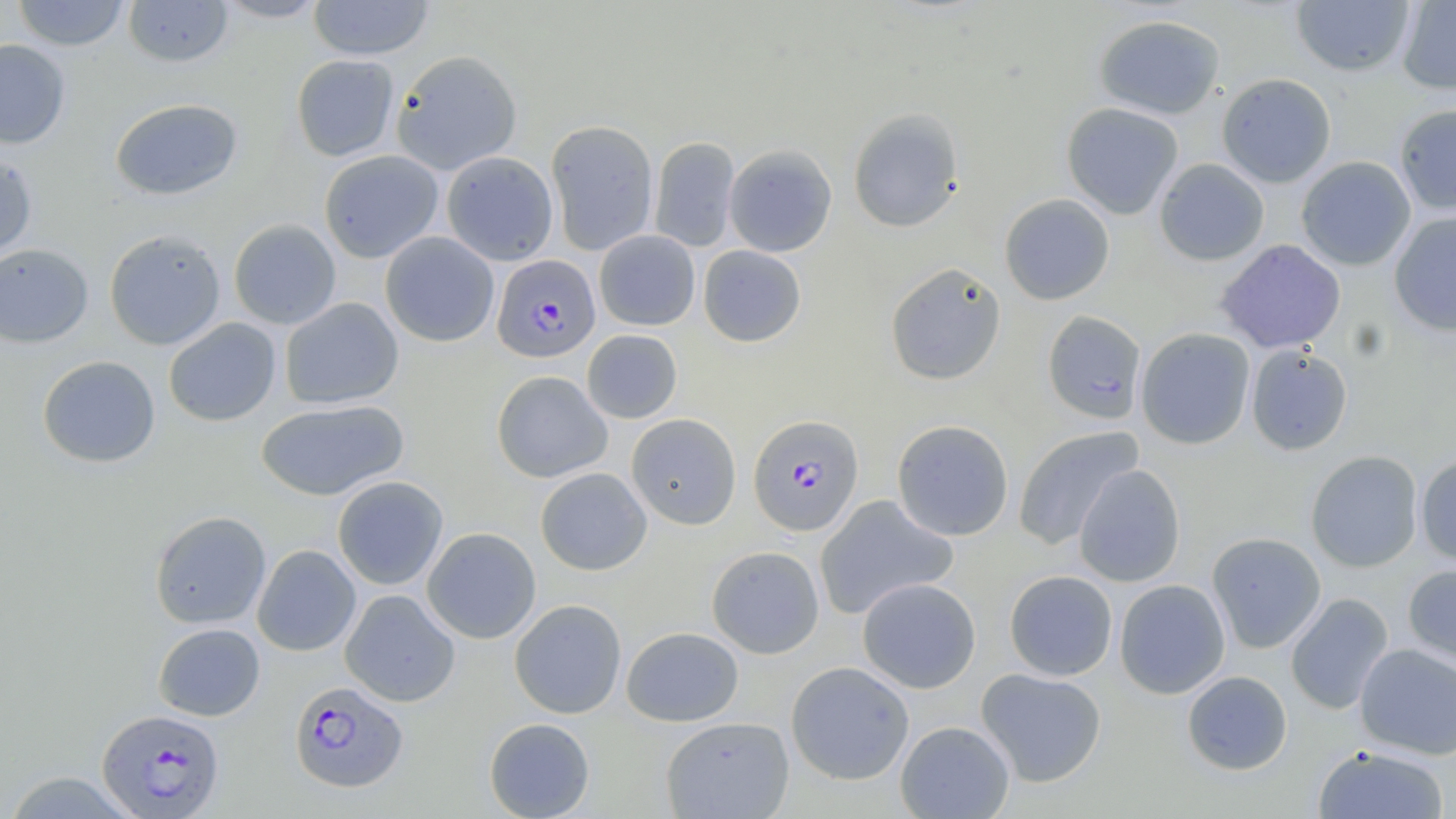
slide_level_diagnosis: Plasmodium falciparum
preparation: thin blood film
field_of_view: one of a larger specimen
plasmodium_falciparum_infected_red_blood_cell_locations: 'approximate bounding boxes as (x1,y1)-(x2,y2) corner pairs in pixels: (492,255)-(600,362), (748,414)-(864,537), (289,680)-(408,792), (97,708)-(225,817)'
magnification: 1000x
image_size: 1456×819 pixels
uninfected_red_blood_cell_locations: 'approximate bounding boxes as (x1,y1)-(x2,y2) corner pairs in pixels: (12,0)-(130,51), (122,0)-(234,68), (212,0)-(330,22), (308,0)-(434,60), (1290,1)-(1415,76), (1396,1)-(1456,95), (1093,14)-(1226,119), (0,39)-(71,149), (391,49)-(522,175), (291,54)-(399,162), (1216,73)-(1337,187), (110,97)-(243,200), (1061,102)-(1184,219), (1394,103)-(1456,215), (847,107)-(965,233), (545,119)-(659,256), (649,136)-(741,253), (724,144)-(837,257), (319,150)-(443,263), (0,151)-(39,262), (441,151)-(558,265), (1296,156)-(1416,271), (1154,158)-(1269,266), (999,193)-(1115,305), (1389,211)-(1456,337), (228,219)-(341,330), (104,229)-(227,350), (594,230)-(700,331), (380,231)-(499,347), (1215,239)-(1346,354), (0,243)-(94,348), (698,245)-(806,347), (885,262)-(1006,385), (279,297)-(404,409), (1042,310)-(1147,424), (163,317)-(281,426), (1136,328)-(1255,450), (581,329)-(682,424), (1245,345)-(1352,455), (36,355)-(161,468), (491,370)-(613,483), (255,398)-(409,502), (626,413)-(741,529), (891,419)-(1014,541), (1012,425)-(1143,549), (1305,451)-(1423,572), (1415,455)-(1456,566), (1073,464)-(1186,587), (535,467)-(652,575), (332,476)-(448,590), (814,495)-(959,620), (149,510)-(271,629), (422,527)-(541,643), (1206,532)-(1326,653), (252,544)-(361,656), (706,545)-(825,659), (1403,562)-(1456,668), (1003,570)-(1118,681), (857,577)-(981,694), (1114,579)-(1231,699), (340,589)-(460,707), (1285,593)-(1394,715), (509,598)-(627,719), (152,622)-(265,721), (621,626)-(744,727), (1355,644)-(1455,759), (785,661)-(914,785), (976,667)-(1107,787), (1182,670)-(1292,776), (660,716)-(794,819), (484,717)-(595,819), (895,720)-(1014,818), (1312,744)-(1449,819), (2,771)-(141,817)'
stain: May-Grünwald-Giemsa
modality: light microscopy